Name the parasite shown.
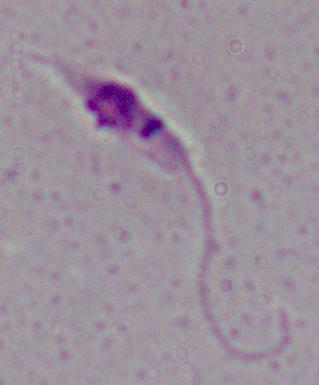

Leishmania.

modality: micrograph
magnification: 1000x